Assess this cell for malaria.
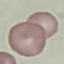
Uninfected.

Thin smear of blood. Automatically extracted cell patch, resized to 64 × 64 pixels. Giemsa stain. Photographed with a smartphone camera at the microscope eyepiece.